Comment on the morphology of the red blood cells.
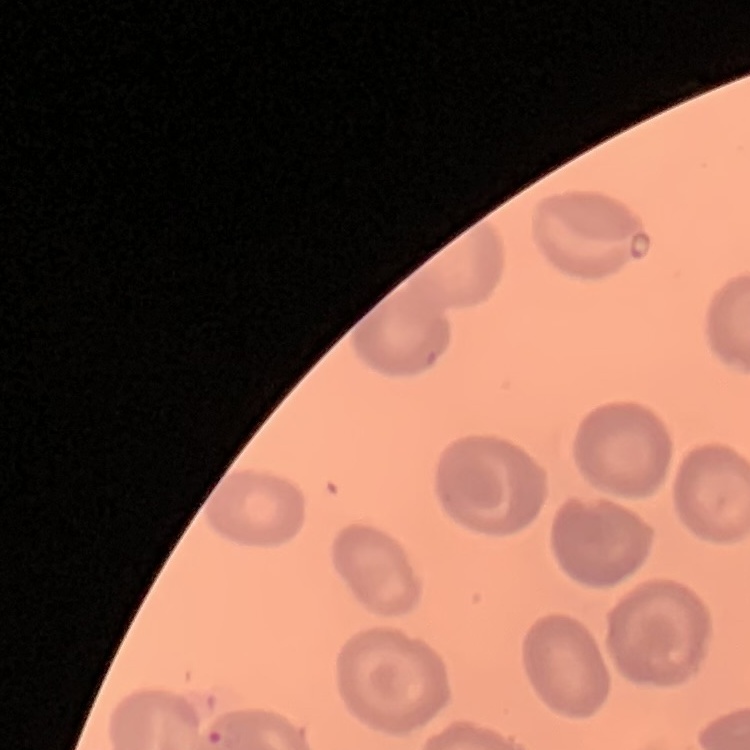
No rouleaux formation.

Summary:
  - Preparation: thin blood smear
  - Image type: square crop of a larger photomicrograph
  - Stain: Field's or Giemsa